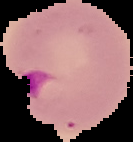
malaria status = parasitized
preparation = thin blood smear
image size = 133×142 pixels
image type = segmented cell region on a black background